Mark where platelets are.
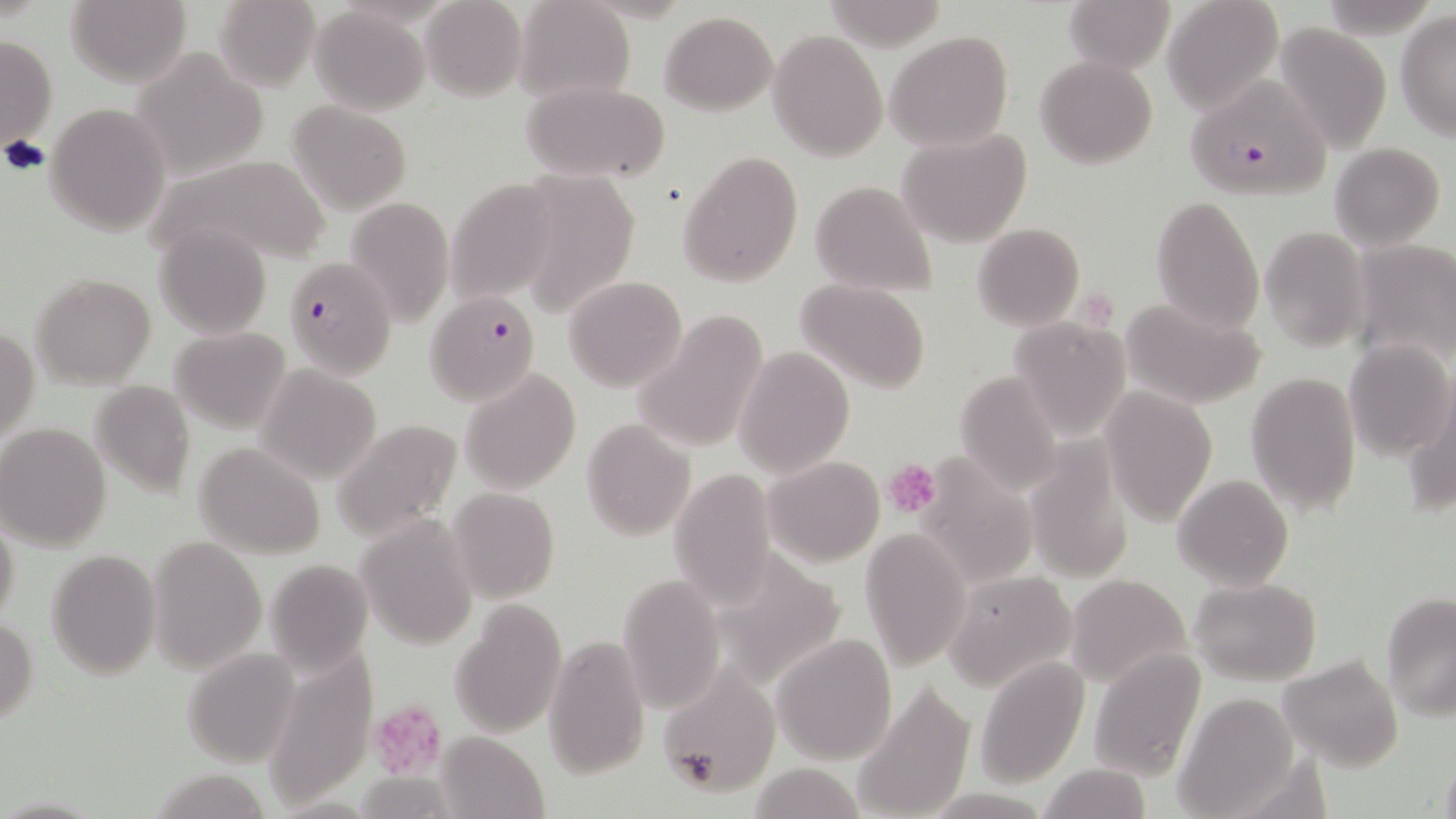
Approximate bounding boxes as (x1,y1)-(x2,y2) corner pairs in pixels.
Platelets: (1077,288)-(1117,332), (884,459)-(941,519), (369,701)-(448,778).

Uninfected red blood cell locations: (65,0)-(191,87), (213,0)-(320,91), (420,0)-(526,102), (1064,0)-(1171,73), (1163,0)-(1284,115), (513,1)-(635,104), (311,6)-(429,115), (1395,10)-(1455,140), (660,11)-(778,116), (1273,23)-(1392,154), (768,30)-(888,162), (885,30)-(1013,153), (1,36)-(57,151), (129,47)-(271,178), (1036,56)-(1157,170), (520,78)-(670,184), (289,101)-(412,214), (45,103)-(170,236), (898,131)-(1032,248), (1329,142)-(1446,252), (678,150)-(804,287), (153,155)-(332,267), (536,164)-(648,318), (445,178)-(555,304), (810,181)-(937,299), (343,193)-(456,323), (1151,194)-(1265,333), (972,222)-(1085,331), (152,225)-(272,339), (1259,226)-(1371,353), (1349,238)-(1456,368), (30,273)-(158,388), (564,275)-(688,391), (796,278)-(931,393), (1119,296)-(1268,410), (634,309)-(768,456), (1009,317)-(1129,439), (1,326)-(38,441), (170,327)-(291,431), (1343,340)-(1455,460), (735,347)-(855,477), (257,365)-(380,480), (460,369)-(580,495), (951,371)-(1065,492), (1245,371)-(1361,515), (88,380)-(196,499), (1099,387)-(1218,525), (1406,392)-(1456,519), (331,417)-(464,542), (580,420)-(695,540), (1,422)-(114,551), (1025,437)-(1135,585), (195,442)-(326,558), (924,456)-(1038,594), (765,457)-(883,566), (667,468)-(778,608), (1172,474)-(1293,591), (447,487)-(559,603), (355,511)-(478,651), (0,513)-(20,631), (860,529)-(971,670), (147,538)-(264,670), (724,546)-(857,680), (46,549)-(160,679), (264,557)-(374,674), (616,571)-(723,713), (942,572)-(1078,693), (1066,574)-(1192,687), (1190,577)-(1322,684), (1382,592)-(1456,719), (450,601)-(567,736), (0,618)-(38,725), (770,633)-(897,765), (544,636)-(650,777), (1089,646)-(1207,781), (181,650)-(300,766), (267,653)-(375,807), (1278,654)-(1403,770), (974,656)-(1088,789), (659,667)-(780,796), (853,683)-(975,818), (1172,694)-(1299,817), (435,731)-(548,817), (1439,753)-(1456,819), (750,762)-(865,819), (1039,762)-(1152,818), (148,768)-(270,819). Plasmodium falciparum-infected red blood cell locations: (1188,76)-(1335,201), (282,256)-(397,378), (426,288)-(540,405). Slide-level diagnosis: Plasmodium falciparum. Single field of view. Light microscopy. Captured at 1000x magnification. May-Grünwald-Giemsa-stained preparation. Thin blood film. Image is 1456×819 pixels.